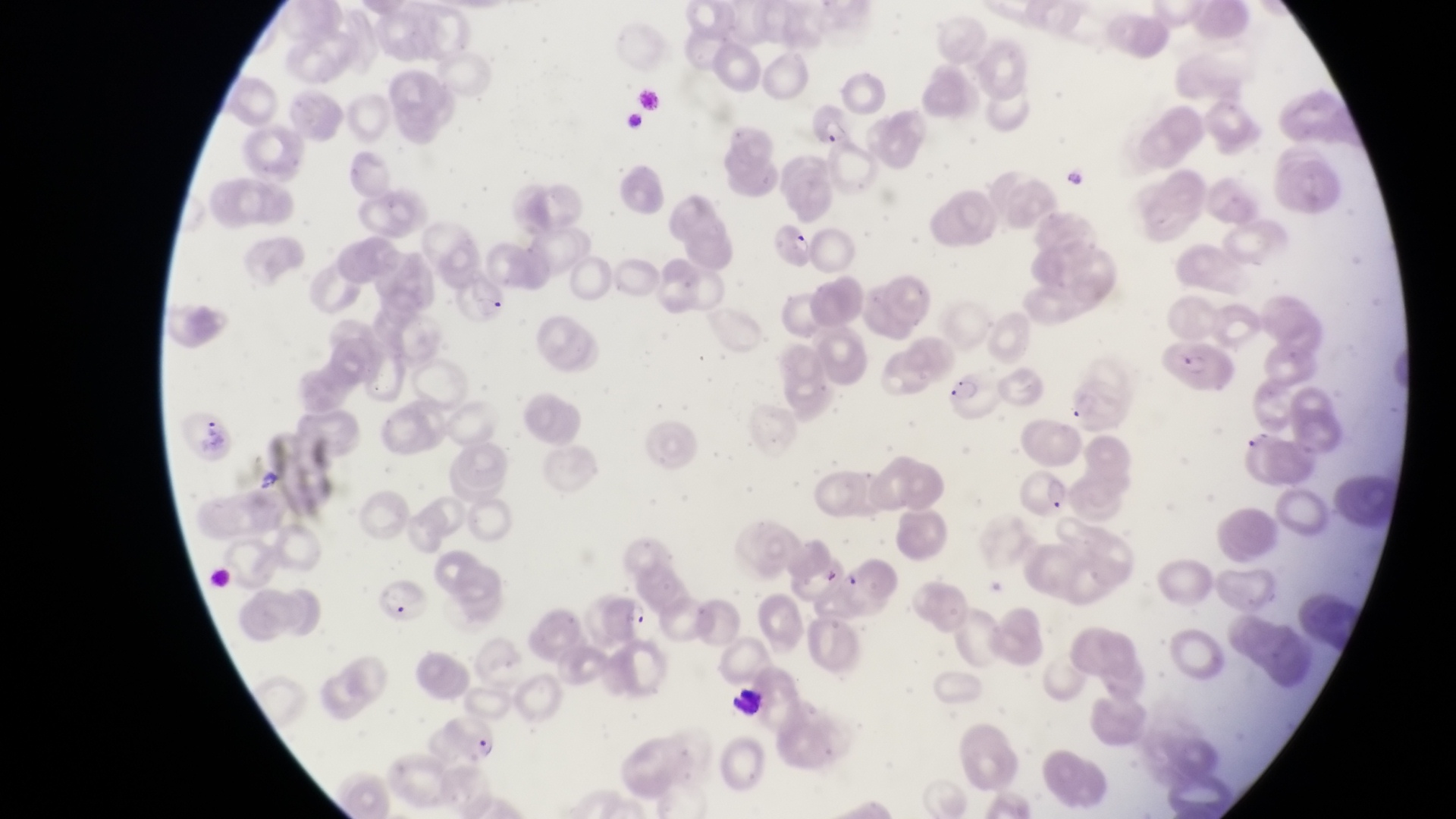
Approximate bounding boxes as (left, top, right, bottom) in pixels. Trophozoite locations: (621, 601, 648, 628). Leukocyte locations: (726, 677, 763, 723). Parasitised red blood cell locations: (812, 103, 854, 148), (764, 215, 819, 271), (450, 277, 510, 330), (1169, 341, 1238, 401), (944, 373, 997, 425), (1065, 375, 1126, 433), (190, 410, 239, 462), (1012, 465, 1071, 526), (376, 578, 434, 628), (444, 714, 503, 764). Collected in Uganda. Captured by a smartphone held over the eyepiece of an Olympus CX-23 microscope. At a magnification of 1000x. Image is 1456×819 pixels. Single field of view. Thin blood smear.